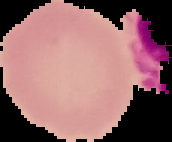

Cell region segmented out of the field of view; the surrounding area is masked to black. Result: negative for malaria parasites. From a thin blood film. Image is 172×142 pixels.